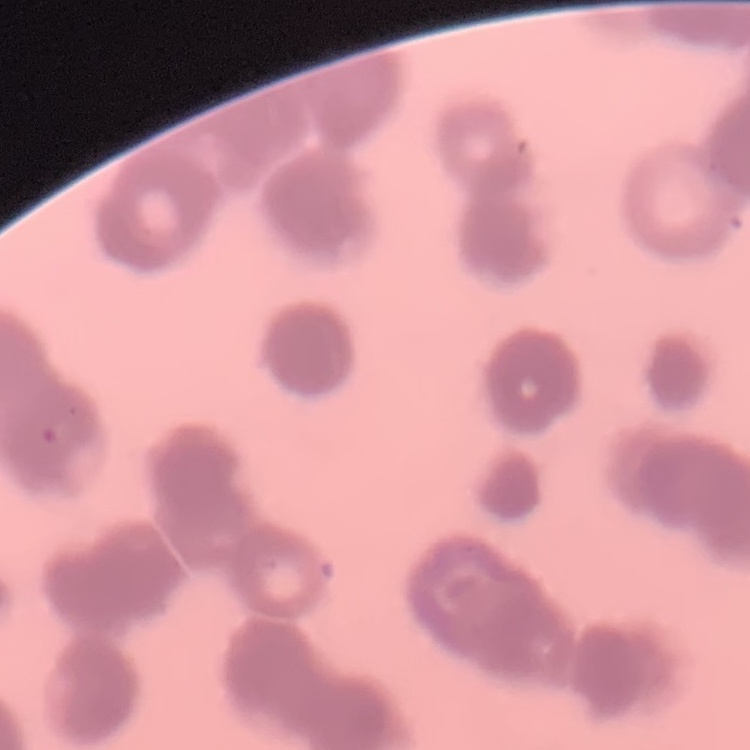 The erythrocytes show rouleaux formation. Field's or Giemsa stain. Thin blood film. Square crop of a larger photomicrograph.